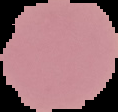

image_type: cell region segmented out of the field of view; surrounding area masked to black
image_size: 118×112 pixels
result: no malaria parasites seen
preparation: thin blood smear